State which cell type is depicted.
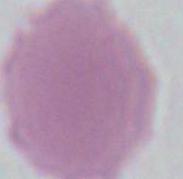

This is an erythrocyte.

Captured at 1000x magnification. Micrograph.